Locate every Plasmodium parasite and every leukocyte.
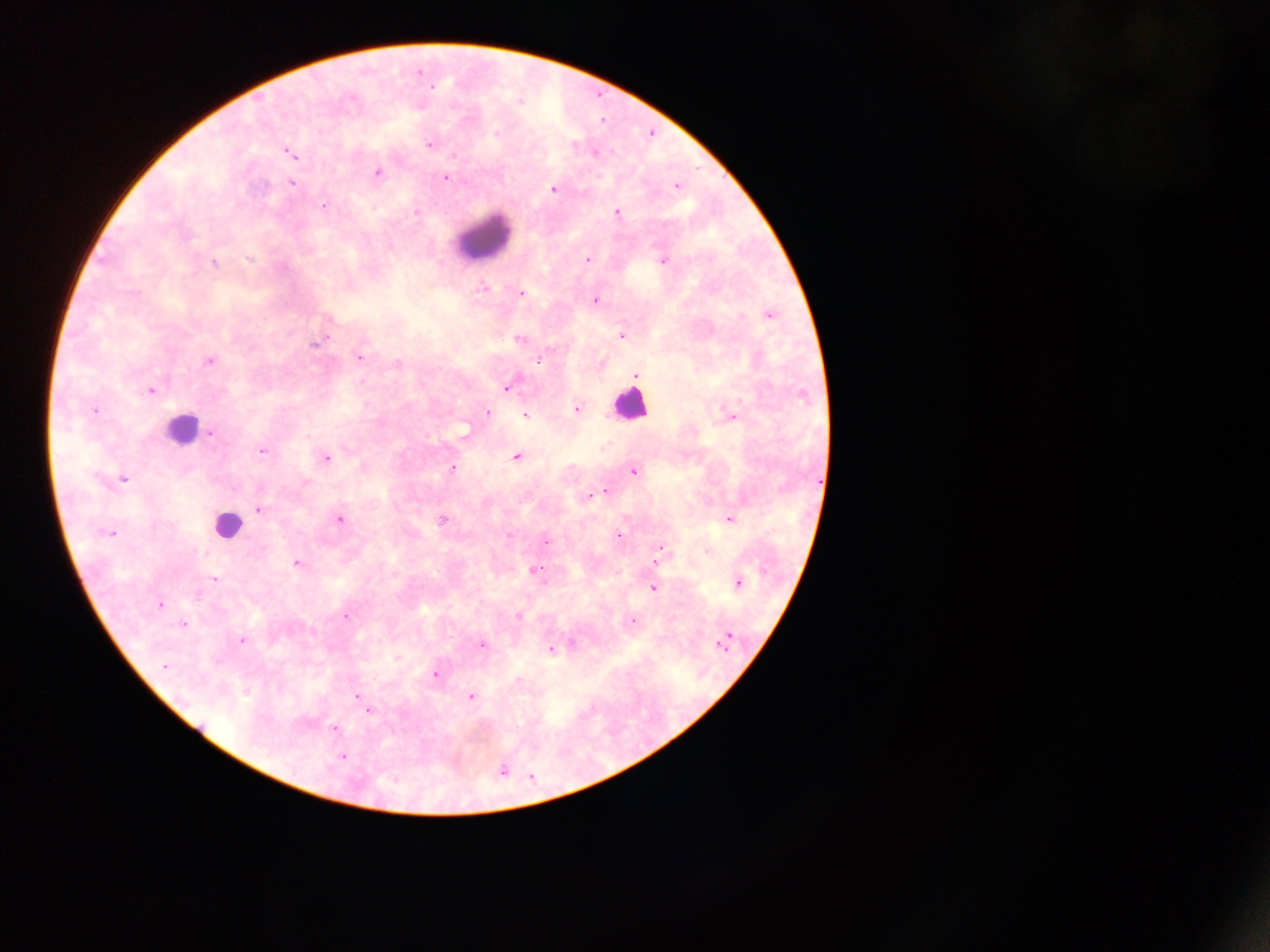

Approximate centers as (x, y) in pixels.
Plasmodium parasites: (430, 86), (429, 144), (288, 152), (593, 153), (377, 173), (445, 178), (291, 182), (677, 185), (553, 188), (324, 205), (617, 212), (587, 260), (664, 260), (213, 262), (484, 288), (521, 293), (594, 300), (767, 313), (622, 335), (520, 338), (315, 342), (359, 357), (538, 359), (208, 360), (397, 363), (636, 374), (506, 386), (149, 390), (576, 407), (94, 409), (486, 411), (525, 414), (730, 416), (210, 434), (262, 450), (325, 457), (516, 457), (452, 469), (633, 471), (123, 478), (605, 491), (596, 493), (589, 496), (258, 509), (729, 518), (339, 519), (441, 520), (111, 532), (510, 535), (618, 535), (545, 541), (660, 548), (707, 551), (656, 561), (297, 563), (534, 570), (213, 579), (737, 583), (653, 587), (159, 605), (345, 614), (518, 616), (631, 621), (183, 623), (726, 639), (241, 640), (480, 644), (551, 648), (164, 666), (435, 675), (471, 695), (356, 696), (368, 710), (334, 728), (342, 756), (501, 770).
Leukocytes: (484, 237), (629, 405), (181, 429), (226, 524).

Summary:
  - Image size: 1270×952 pixels
  - Capture: mobile-phone photograph through a microscope
  - Country: Ghana
  - Preparation: thick blood film
  - Field of view: single